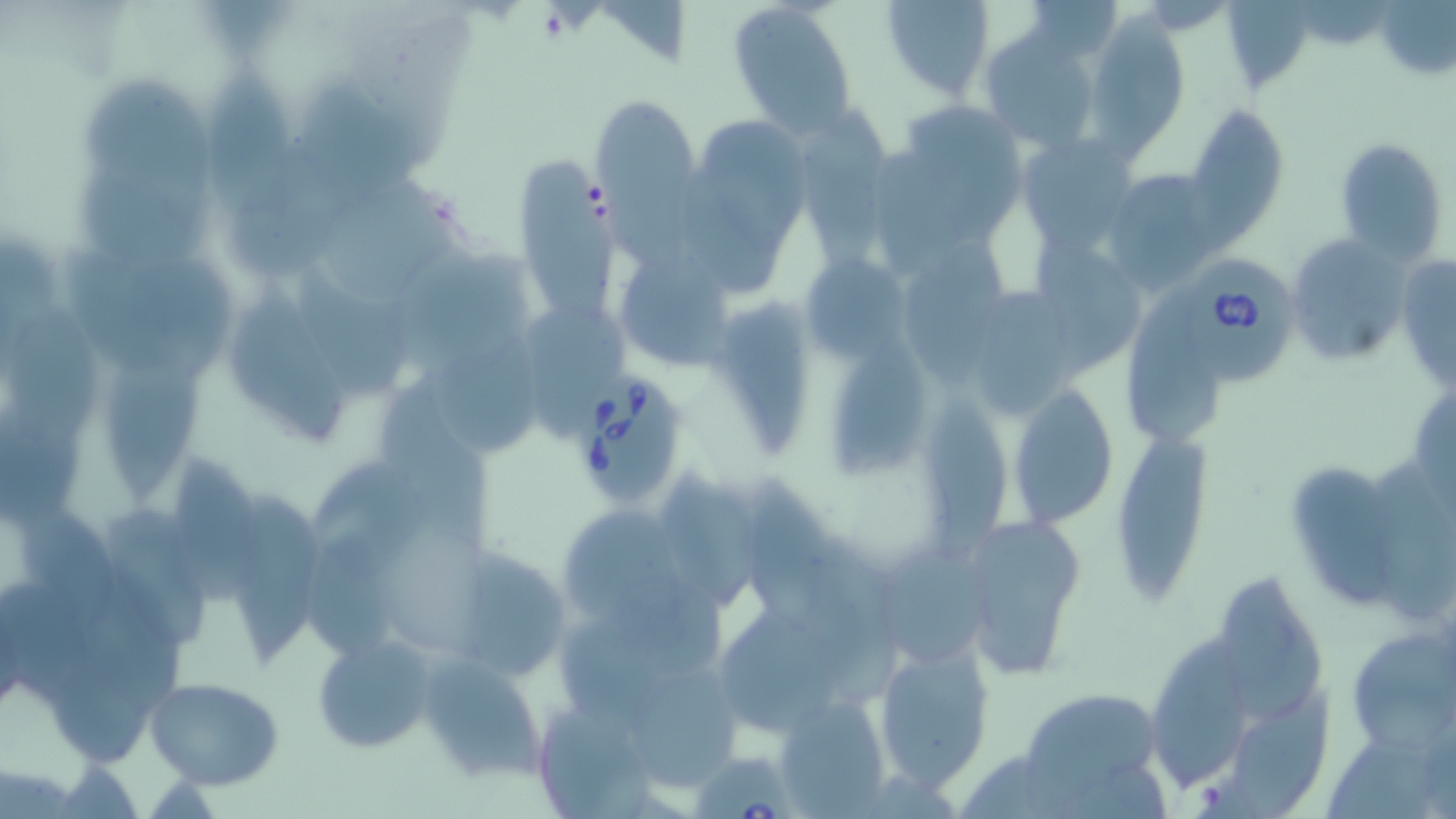
slide-level diagnosis = Babesia divergens
preparation = thin blood film
field of view = single
modality = optical microscopy
stain = May-Grünwald-Giemsa
magnification = 1000x
image size = 1456×819 pixels
uninfected red blood cell locations = approximate bounding boxes as (x1, y1, x2, y2) in pixels: (727, 0, 859, 137), (880, 0, 996, 100), (1024, 1, 1123, 63), (1085, 15, 1188, 156), (982, 27, 1105, 157), (211, 62, 301, 213), (81, 79, 213, 207), (302, 91, 421, 196), (602, 95, 698, 275), (796, 104, 886, 266), (1184, 104, 1289, 237), (905, 106, 1021, 243), (709, 122, 813, 249), (1018, 135, 1138, 250), (1334, 136, 1449, 264), (227, 140, 345, 281), (870, 143, 949, 281), (521, 157, 621, 317), (1100, 169, 1225, 294), (80, 172, 212, 284), (686, 174, 783, 293), (322, 175, 464, 299), (1288, 231, 1408, 366), (907, 232, 1008, 390), (1038, 238, 1147, 371), (394, 251, 535, 379), (1395, 254, 1455, 395), (120, 259, 236, 368), (623, 259, 732, 370), (803, 260, 906, 356), (297, 268, 411, 400), (228, 281, 349, 439), (971, 283, 1075, 416), (1123, 288, 1230, 440), (715, 298, 808, 454), (12, 305, 100, 445), (526, 312, 632, 435), (439, 336, 543, 459), (833, 341, 943, 480), (107, 344, 207, 507), (1011, 383, 1123, 528), (922, 386, 1011, 556), (382, 388, 494, 552), (0, 409, 86, 527), (1112, 429, 1212, 595), (177, 452, 261, 611), (1289, 457, 1400, 610), (317, 458, 429, 581), (746, 468, 841, 626), (665, 472, 769, 606), (226, 493, 324, 677), (15, 501, 122, 636), (108, 509, 217, 654), (561, 511, 685, 618), (961, 517, 1090, 682), (379, 524, 498, 659), (814, 529, 908, 706), (307, 534, 398, 657), (881, 545, 987, 662), (443, 547, 574, 683), (612, 565, 736, 683), (1221, 570, 1329, 727), (78, 594, 190, 704), (558, 610, 668, 718), (719, 610, 827, 739), (1349, 628, 1455, 754), (312, 633, 440, 754), (1147, 633, 1252, 792), (872, 635, 995, 792), (417, 652, 548, 785), (50, 664, 154, 770), (632, 675, 745, 794), (143, 677, 285, 789), (1020, 688, 1163, 799), (528, 694, 663, 817), (772, 694, 889, 816)
Babesia divergens-infected red blood cell locations = approximate bounding boxes as (x1, y1, x2, y2) in pixels: (1181, 256, 1300, 393), (565, 375, 691, 504), (691, 747, 798, 817)